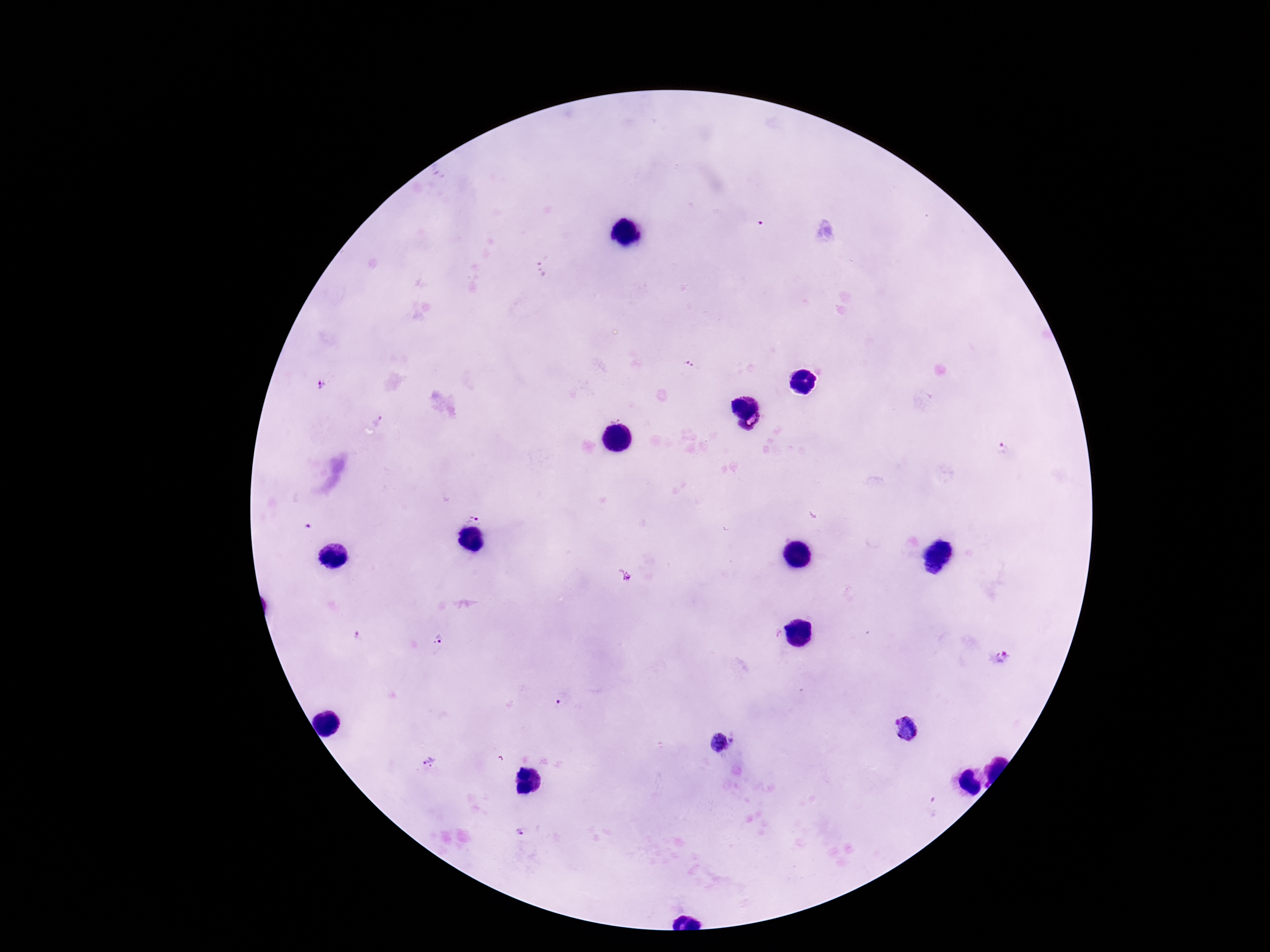

Approximate object centers, in pixels from the top-left corner. Plasmodium parasite locations: (x=688, y=363), (x=321, y=386), (x=378, y=422), (x=749, y=422), (x=1001, y=449), (x=473, y=518), (x=623, y=575), (x=358, y=635), (x=440, y=639), (x=1002, y=658), (x=559, y=701), (x=906, y=727), (x=722, y=742), (x=430, y=762). Giemsa-stained preparation. One field from this slide. Thick blood film. Smartphone photograph taken through the microscope eyepiece. Patient malaria status: infected. Image is 1270×952 pixels. 100x magnification.